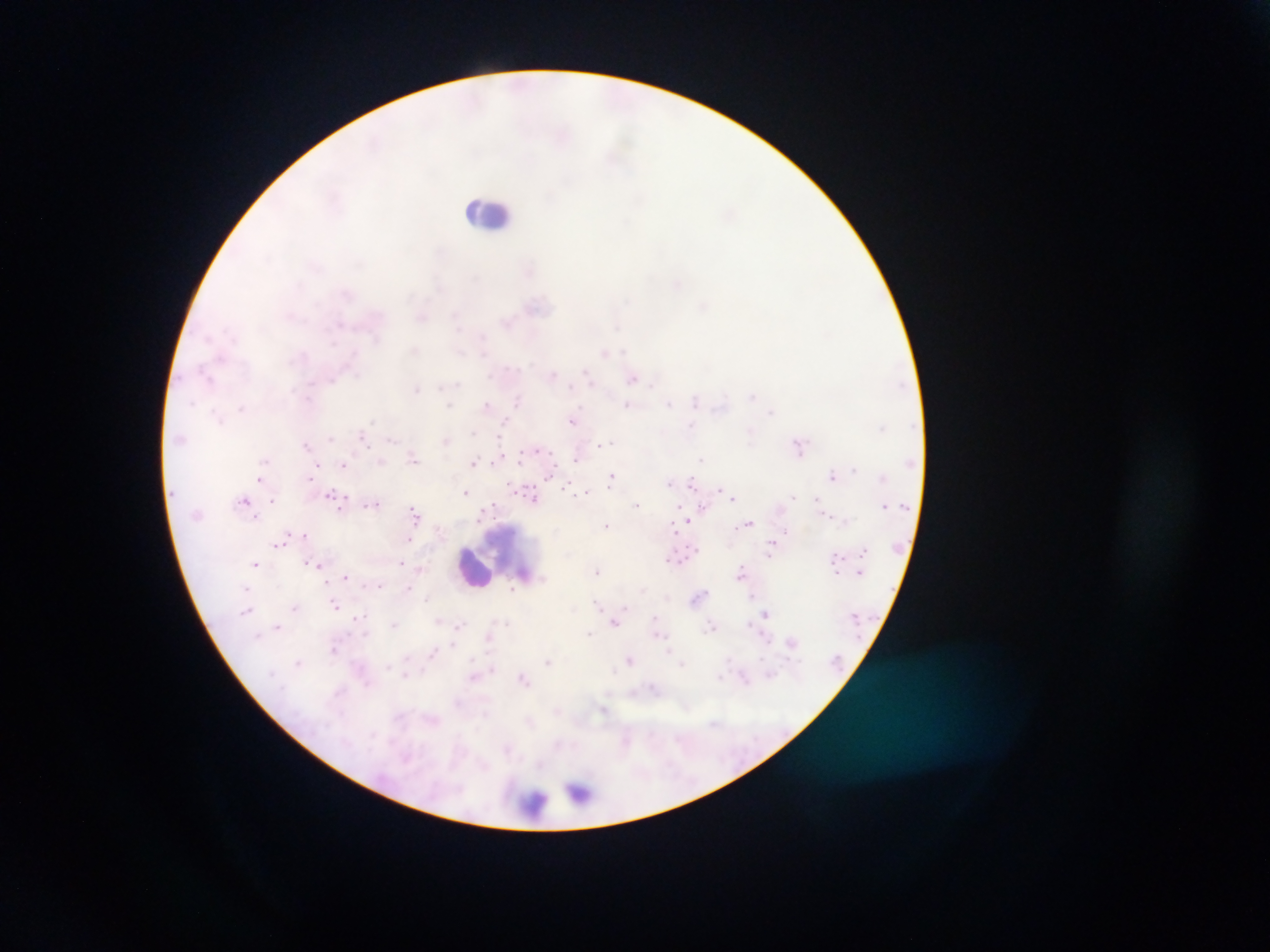
Approximate centers as [x, y] in pixels. Leukocyte locations: [485, 210], [474, 569]. Malaria parasite locations: [618, 326], [481, 336], [622, 348], [483, 355], [589, 379], [632, 380], [652, 384], [440, 385], [457, 385], [571, 385], [418, 388], [752, 397], [520, 400], [695, 402], [670, 403], [448, 404], [486, 404], [628, 404], [505, 421], [571, 422], [691, 426], [363, 430], [473, 431], [329, 437], [392, 440], [447, 440], [606, 442], [305, 445], [602, 445], [536, 449], [413, 457], [497, 458], [575, 458], [702, 458], [265, 459], [519, 459], [344, 462], [381, 462], [472, 462], [318, 463], [853, 469], [613, 474], [549, 475], [309, 476], [831, 476], [259, 479], [670, 482], [692, 483], [569, 487], [718, 489], [586, 491], [330, 492], [464, 492], [534, 498], [734, 498], [246, 499], [272, 500], [376, 503], [638, 504], [493, 505], [882, 505], [414, 509], [481, 515], [827, 515], [687, 521], [749, 523], [608, 526], [670, 530], [787, 530], [304, 533], [410, 538], [279, 546], [837, 556], [671, 561], [400, 562], [256, 563], [305, 563], [317, 563], [421, 568], [740, 570], [863, 570], [598, 575], [345, 576], [513, 587], [407, 588], [644, 591], [335, 604], [294, 606], [627, 606], [247, 611], [766, 613], [654, 616], [393, 623], [614, 623], [749, 624], [278, 626], [712, 627], [333, 652], [473, 660], [630, 660], [298, 661], [682, 664], [270, 671], [613, 672]. Image is 1270×952 pixels. Thick blood film. Single field of view. Mobile-phone photograph taken through the microscope. Collected in Ghana.